Point out each malaria parasite.
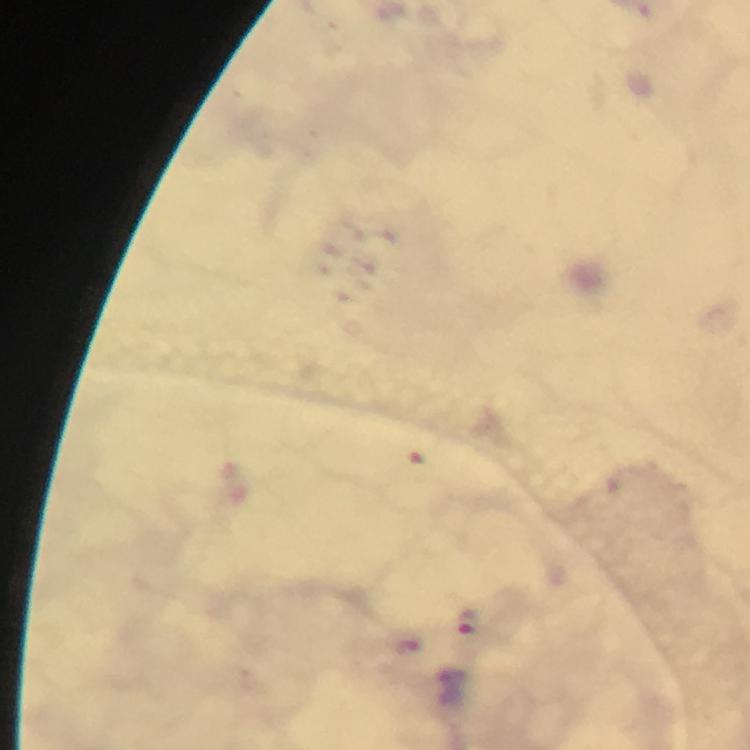
Approximate centers as (x, y) in pixels.
Malaria parasites: (468, 621), (406, 649).

Cropped region of a single field of view. Giemsa stain. Photographed through the microscope with a smartphone camera. At 100x magnification. Immersion oil applied. Image is 750×750 pixels. From a malaria diagnostic workup. Thick smear.